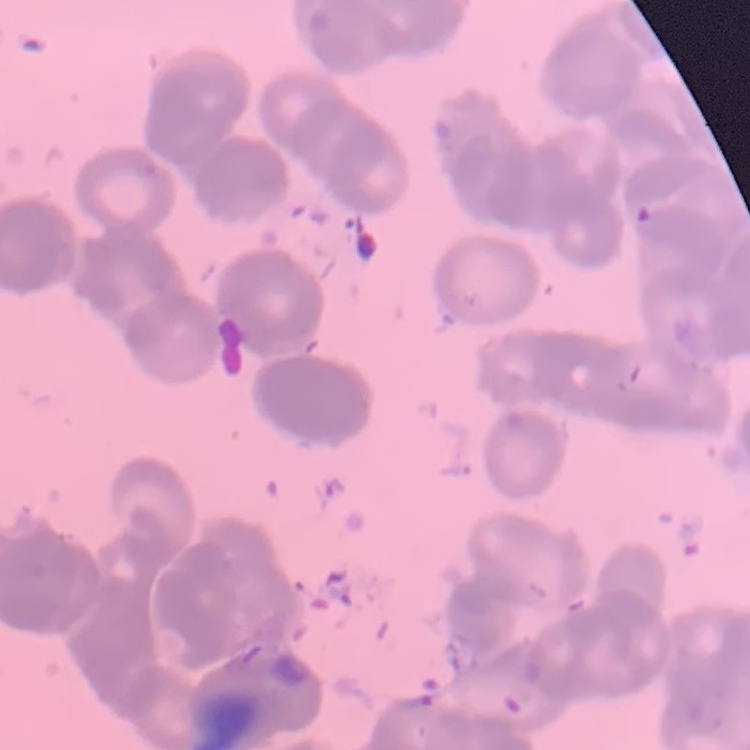

The red blood cells exhibit rouleaux formation. Field's or Giemsa stain. Square crop of a larger photomicrograph. Thin peripheral smear.